Report the malaria status of this cell.
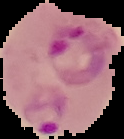
Parasitized.

Summary:
  - Preparation: thin blood smear
  - Image size: 124×139 pixels
  - Image type: segmented cell region on a black background